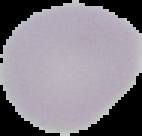
image size = 142×136 pixels
image type = segmented cell region on a black background
preparation = thin blood smear
result = no Plasmodium parasites seen